Identify the blood parasite species.
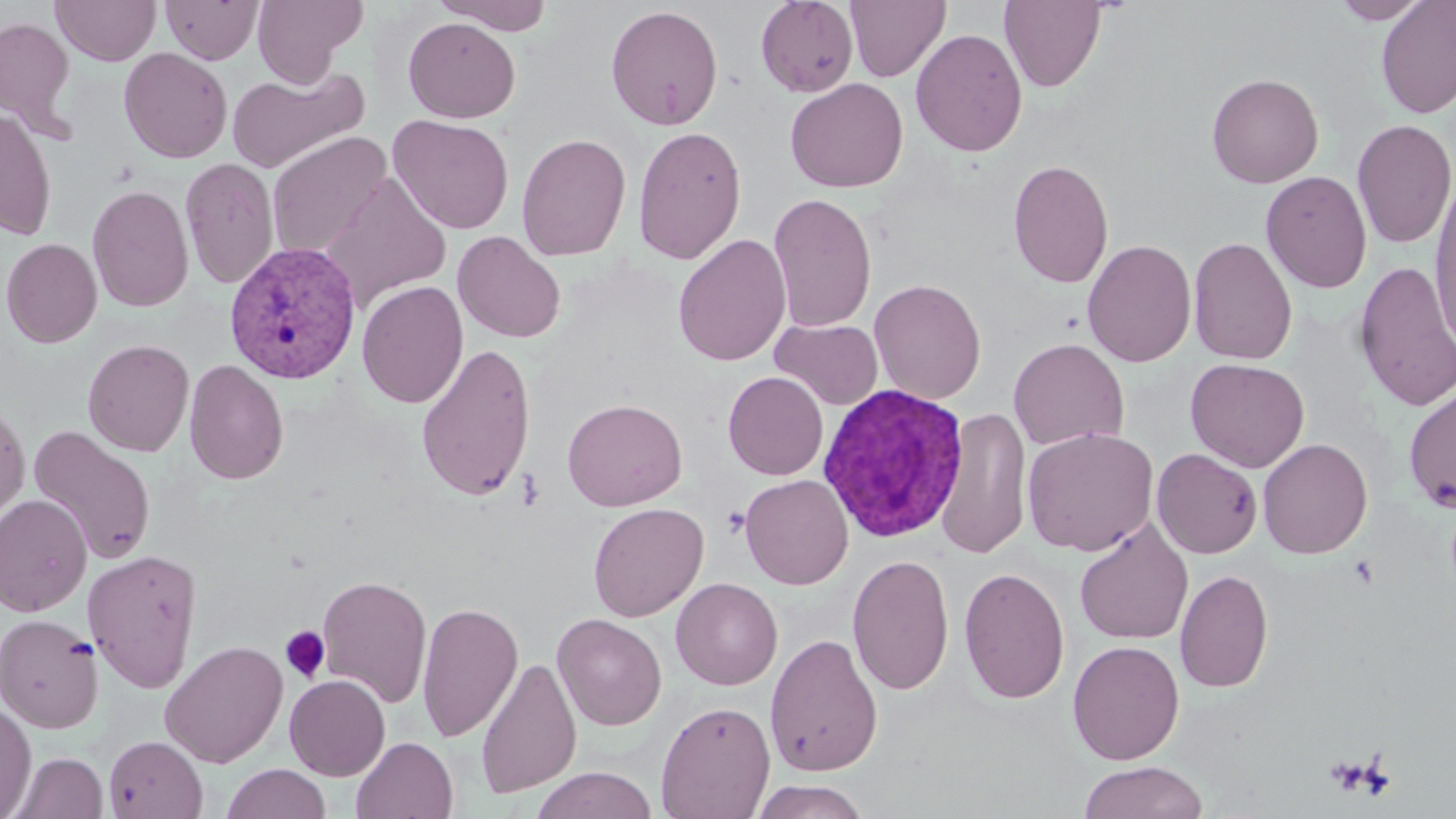

Plasmodium vivax.

Approximate bounding boxes as [x1, y1, x2, y2] in pixels. Platelet locations: [518, 467, 543, 510], [722, 507, 749, 537], [280, 626, 330, 683]. Plasmodium vivax-infected red blood cell locations: [223, 242, 362, 384], [815, 383, 970, 543]. Uninfected red blood cell locations: [51, 0, 161, 66], [252, 0, 366, 86], [433, 0, 555, 35], [755, 0, 858, 97], [1329, 0, 1433, 24], [1376, 0, 1456, 119], [161, 1, 263, 64], [845, 1, 951, 82], [999, 1, 1107, 92], [605, 4, 724, 131], [0, 16, 76, 135], [402, 17, 521, 123], [911, 28, 1028, 157], [118, 47, 232, 163], [227, 64, 370, 175], [1206, 72, 1324, 188], [785, 77, 908, 193], [0, 108, 57, 241], [388, 114, 514, 234], [1352, 118, 1456, 250], [632, 125, 747, 264], [266, 131, 392, 259], [516, 132, 631, 261], [180, 157, 279, 290], [1007, 158, 1114, 289], [1260, 170, 1372, 294], [321, 173, 452, 311], [1428, 183, 1456, 351], [87, 184, 193, 312], [768, 191, 877, 332], [452, 230, 566, 343], [673, 233, 792, 366], [1188, 236, 1298, 365], [0, 237, 102, 348], [1082, 238, 1196, 367], [1353, 261, 1456, 412], [868, 278, 986, 404], [356, 280, 468, 409], [770, 318, 884, 410], [82, 338, 194, 456], [1008, 338, 1129, 451], [415, 342, 537, 501], [1185, 358, 1310, 472], [184, 359, 289, 485], [723, 371, 828, 480], [1403, 383, 1456, 512], [562, 398, 688, 510], [0, 400, 31, 525], [935, 407, 1032, 560], [27, 425, 157, 565], [1022, 426, 1159, 556], [1257, 438, 1373, 559], [1152, 448, 1262, 558], [740, 474, 853, 590], [0, 494, 92, 616], [588, 502, 708, 622], [1074, 520, 1194, 645], [82, 549, 203, 692], [847, 554, 955, 696], [958, 566, 1071, 704], [1175, 569, 1274, 694], [316, 574, 432, 708], [671, 578, 782, 690], [417, 601, 523, 743], [0, 613, 104, 734], [552, 613, 667, 730], [765, 633, 883, 776], [160, 639, 289, 768], [1067, 640, 1185, 764], [475, 656, 581, 798], [284, 674, 390, 781], [0, 700, 35, 818], [655, 700, 776, 818], [103, 735, 208, 818], [351, 736, 458, 819], [9, 752, 108, 819], [1078, 761, 1208, 819], [222, 764, 331, 819], [531, 767, 658, 819], [749, 780, 872, 818]. Optical microscopy. Image is 1456×819 pixels. 1000x magnification. Thin blood film. One field of a larger specimen. May-Grünwald-Giemsa stain.